Evaluate for malaria.
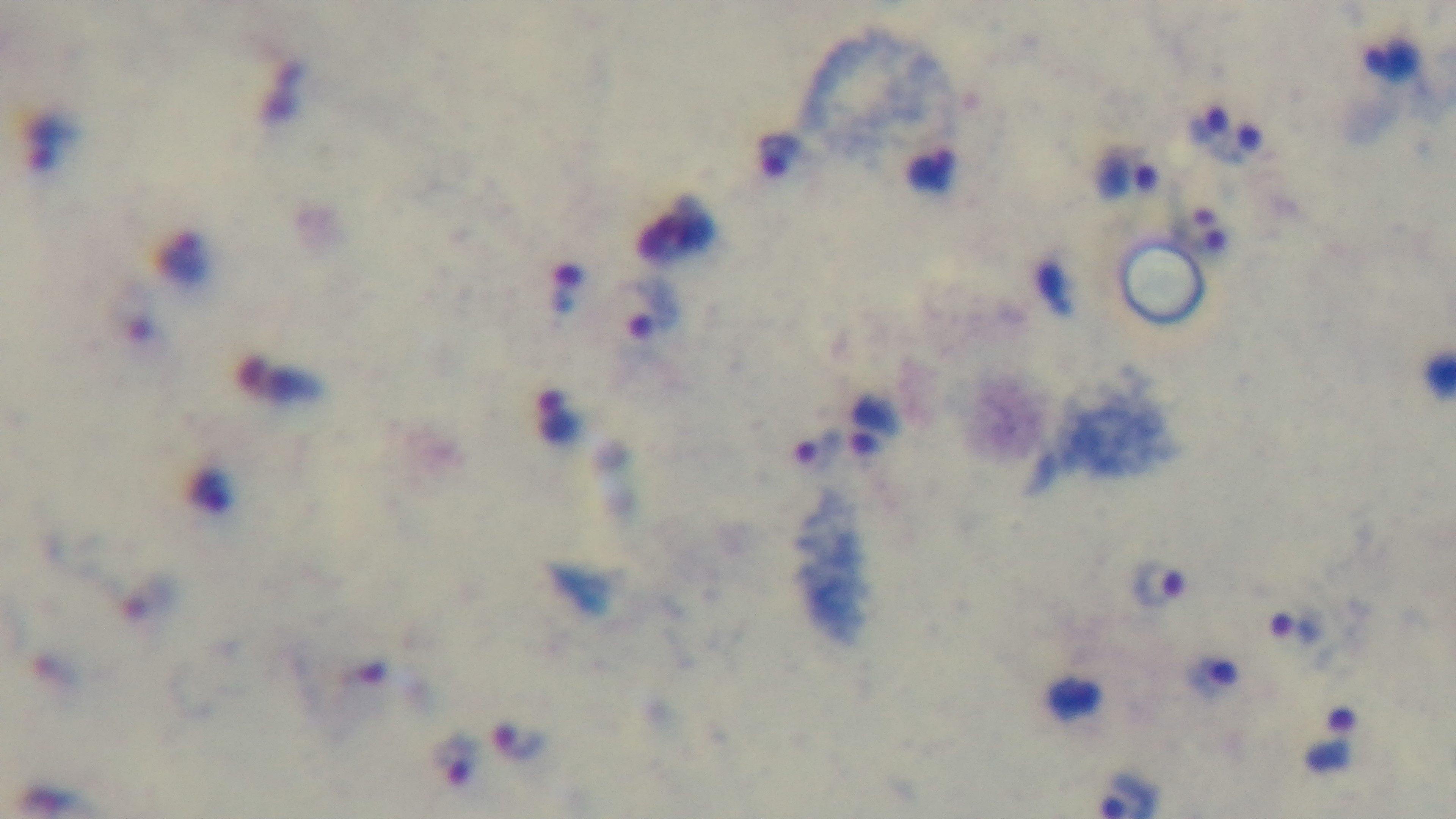
Infected.

preparation = thick blood film
field of view = one from the slide
modality = light microscopy
objective = 100x oil immersion
stain = Giemsa
capture = mounted 4K digital camera